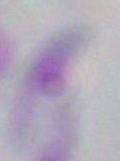
Captured at 1000x magnification. Toxoplasma gondii is shown. Photomicrograph.